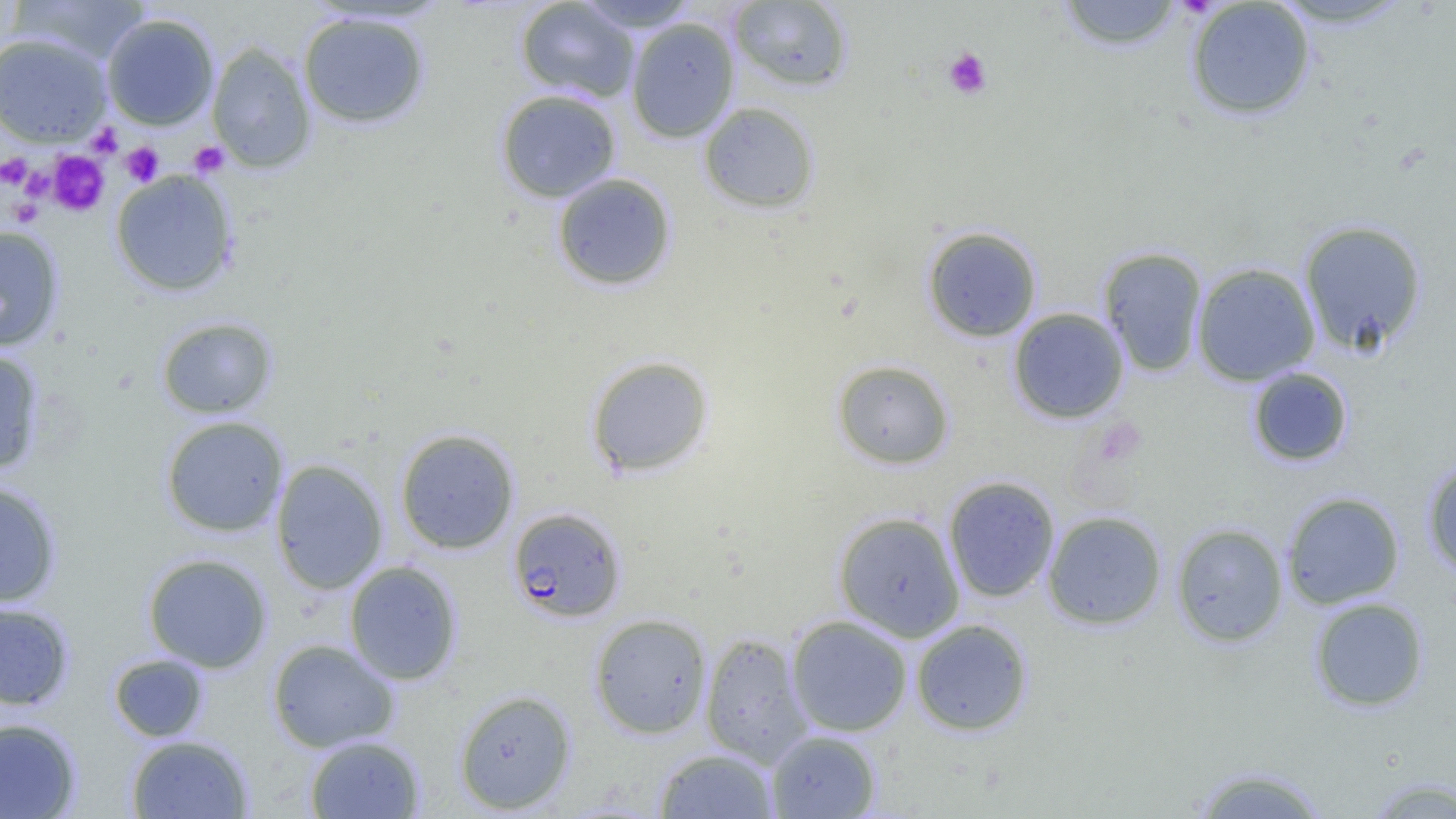 Approximate bounding boxes as named x1/y1/x2/y2 corners in pixels. Plasmodium falciparum-infected red blood cell locations: (x1=507, y1=507, x2=626, y2=622). Platelet locations: (x1=943, y1=47, x2=992, y2=100), (x1=87, y1=123, x2=123, y2=158), (x1=188, y1=141, x2=229, y2=177), (x1=120, y1=142, x2=164, y2=186), (x1=48, y1=151, x2=109, y2=216), (x1=0, y1=152, x2=33, y2=189), (x1=19, y1=163, x2=56, y2=200), (x1=7, y1=198, x2=45, y2=227). Uninfected red blood cell locations: (x1=10, y1=0, x2=150, y2=66), (x1=1056, y1=0, x2=1185, y2=51), (x1=1268, y1=0, x2=1414, y2=29), (x1=515, y1=1, x2=640, y2=103), (x1=574, y1=1, x2=700, y2=33), (x1=729, y1=1, x2=854, y2=92), (x1=1185, y1=2, x2=1316, y2=120), (x1=297, y1=10, x2=431, y2=130), (x1=101, y1=13, x2=220, y2=130), (x1=517, y1=13, x2=739, y2=119), (x1=626, y1=17, x2=740, y2=143), (x1=0, y1=32, x2=112, y2=147), (x1=206, y1=41, x2=317, y2=173), (x1=495, y1=89, x2=621, y2=203), (x1=698, y1=102, x2=820, y2=214), (x1=110, y1=169, x2=239, y2=297), (x1=552, y1=173, x2=677, y2=291), (x1=1298, y1=219, x2=1427, y2=354), (x1=0, y1=225, x2=65, y2=351), (x1=922, y1=225, x2=1042, y2=342), (x1=1098, y1=247, x2=1208, y2=377), (x1=1192, y1=262, x2=1320, y2=385), (x1=1007, y1=308, x2=1129, y2=424), (x1=156, y1=316, x2=278, y2=419), (x1=0, y1=347, x2=46, y2=476), (x1=585, y1=355, x2=715, y2=478), (x1=831, y1=359, x2=955, y2=469), (x1=1247, y1=367, x2=1353, y2=467), (x1=160, y1=415, x2=289, y2=537), (x1=395, y1=428, x2=520, y2=554), (x1=1421, y1=457, x2=1456, y2=578), (x1=270, y1=459, x2=389, y2=595), (x1=943, y1=475, x2=1060, y2=602), (x1=0, y1=481, x2=62, y2=606), (x1=1281, y1=492, x2=1405, y2=609), (x1=833, y1=511, x2=965, y2=642), (x1=1043, y1=511, x2=1167, y2=630), (x1=1171, y1=522, x2=1289, y2=647), (x1=143, y1=553, x2=272, y2=672), (x1=344, y1=560, x2=462, y2=685), (x1=1309, y1=597, x2=1429, y2=712), (x1=0, y1=602, x2=74, y2=710), (x1=589, y1=613, x2=712, y2=739), (x1=786, y1=615, x2=913, y2=737), (x1=911, y1=618, x2=1033, y2=736), (x1=700, y1=632, x2=814, y2=766), (x1=267, y1=638, x2=399, y2=753), (x1=109, y1=654, x2=209, y2=742), (x1=453, y1=689, x2=577, y2=814), (x1=0, y1=717, x2=81, y2=818), (x1=767, y1=730, x2=881, y2=818), (x1=126, y1=734, x2=254, y2=818), (x1=305, y1=734, x2=425, y2=818), (x1=654, y1=748, x2=778, y2=818), (x1=1190, y1=764, x2=1332, y2=818), (x1=1363, y1=776, x2=1456, y2=818). Slide-level diagnosis: Plasmodium falciparum. Thin blood film. 1000x magnification. Image is 1456×819 pixels. Optical microscopy. Single field of view.